Report the malaria status of this cell.
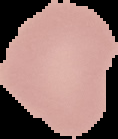
Uninfected.

image type = cell region segmented out of the field of view; surrounding area masked to black
preparation = thin blood smear
image size = 118×139 pixels